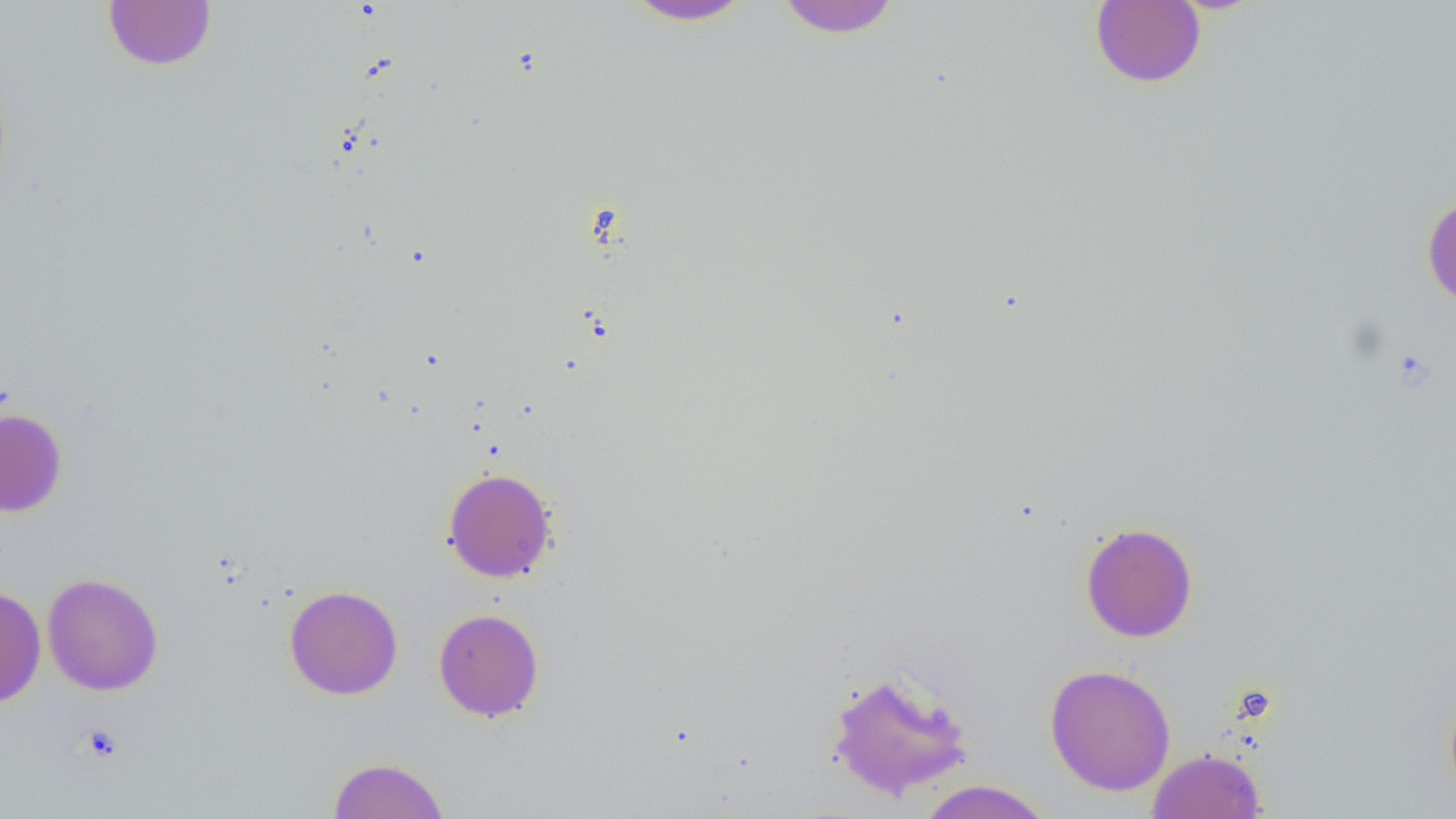 Approximate bounding boxes as (x1,y1)-(x2,y2) corner pairs in pixels. Uninfected red blood cell locations: (619,0)-(759,27), (771,0)-(904,38), (103,1)-(217,71), (1090,1)-(1206,88), (1422,194)-(1456,311), (0,408)-(67,517), (442,468)-(558,583), (1080,521)-(1198,643), (42,572)-(163,696), (0,585)-(46,709), (284,585)-(403,700), (433,608)-(544,721), (1044,663)-(1176,796), (826,669)-(975,802), (1443,683)-(1456,809), (1147,748)-(1267,819), (328,756)-(450,818), (914,780)-(1055,819). Platelet locations: (78,724)-(124,763). Slide-level diagnosis: negative for blood parasites. Image is 1456×819 pixels. Single field of view. 1000x magnification. Thin blood film. Optical microscopy.